Report the malaria status of this cell.
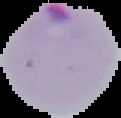
It is parasitized.

image size = 121×118 pixels
preparation = thin blood smear
image type = segmented cell region on a black background